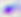

Toxoplasma gondii is seen. Captured at 400x magnification. Photomicrograph.